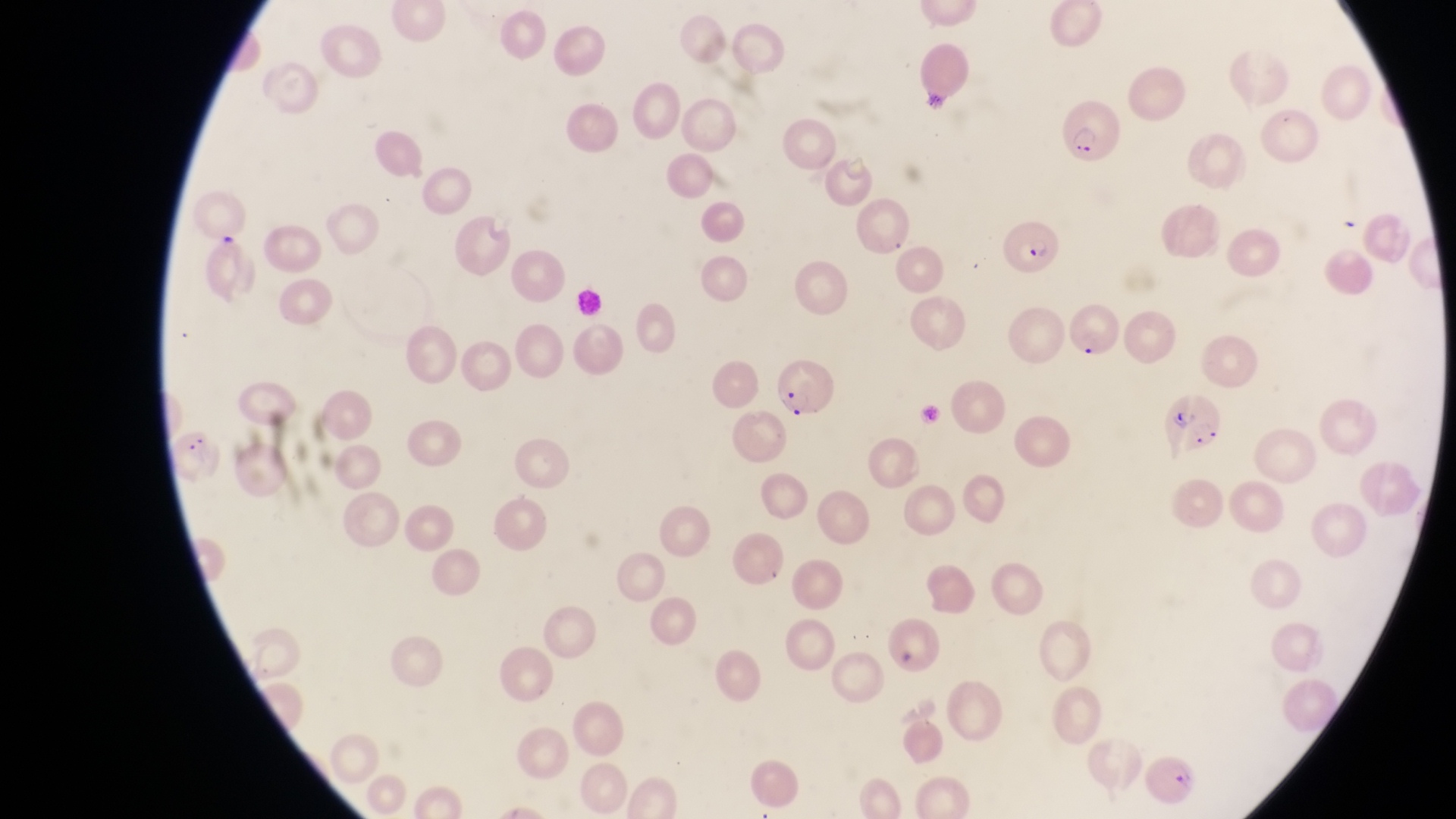
Approximate bounding boxes as left top right bottom in pixels.
Summary:
  - Parasitised red blood cell locations: 1007 219 1059 275; 777 360 840 418; 1159 394 1220 453; 1141 756 1200 802
  - Image size: 1456×819 pixels
  - Magnification: 1000x
  - Field of view: single
  - Capture: smartphone photograph through the eyepiece of an Olympus CX-23 microscope
  - Country: Uganda
  - Preparation: thin blood film